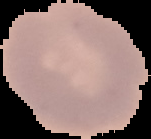

Summary:
  - Image type: cell region segmented out of the field of view; surrounding area masked to black
  - Preparation: thin blood smear
  - Image size: 151×139 pixels
  - Result: no Plasmodium parasites seen